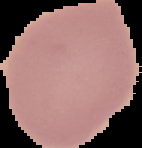
Summary:
  - Malaria status: uninfected
  - Preparation: thin blood smear
  - Image type: cell region segmented out of the field of view; surrounding area masked to black
  - Image size: 142×148 pixels